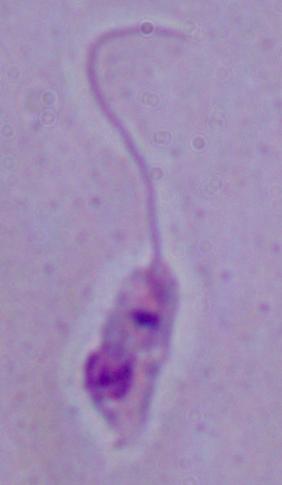

modality = micrograph
identification = Leishmania
magnification = 1000x